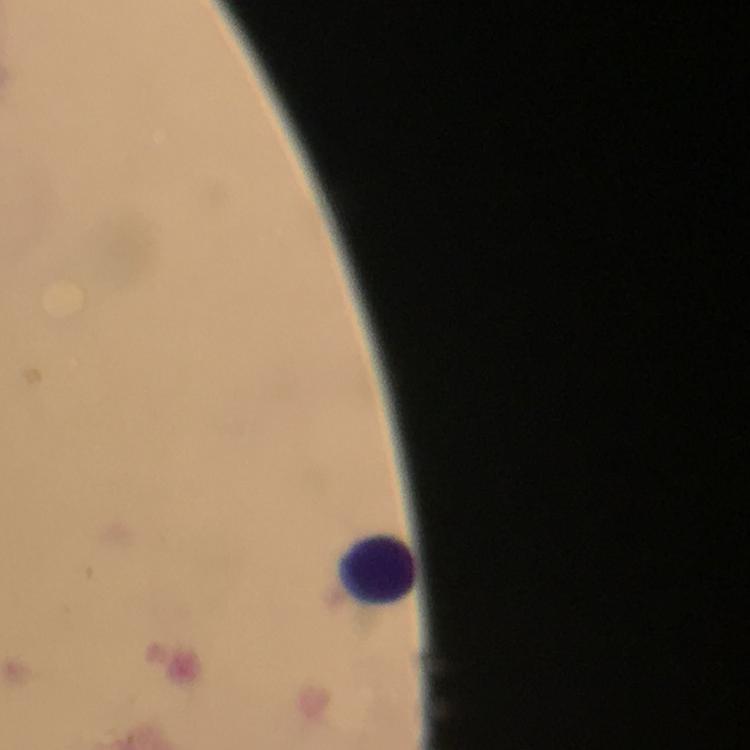

{
  "malaria_parasites": "none seen",
  "context": "from a malaria diagnostic workup",
  "image_size": "750×750 pixels",
  "stain": "Giemsa",
  "preparation": "thick blood film",
  "cropped_from": "a single field of view",
  "magnification": "100x",
  "leukocyte_locations": "approximate object centers, in pixels from the top-left corner: (x=378, y=571)",
  "capture": "smartphone photograph through a microscope",
  "immersion_oil": "used"
}